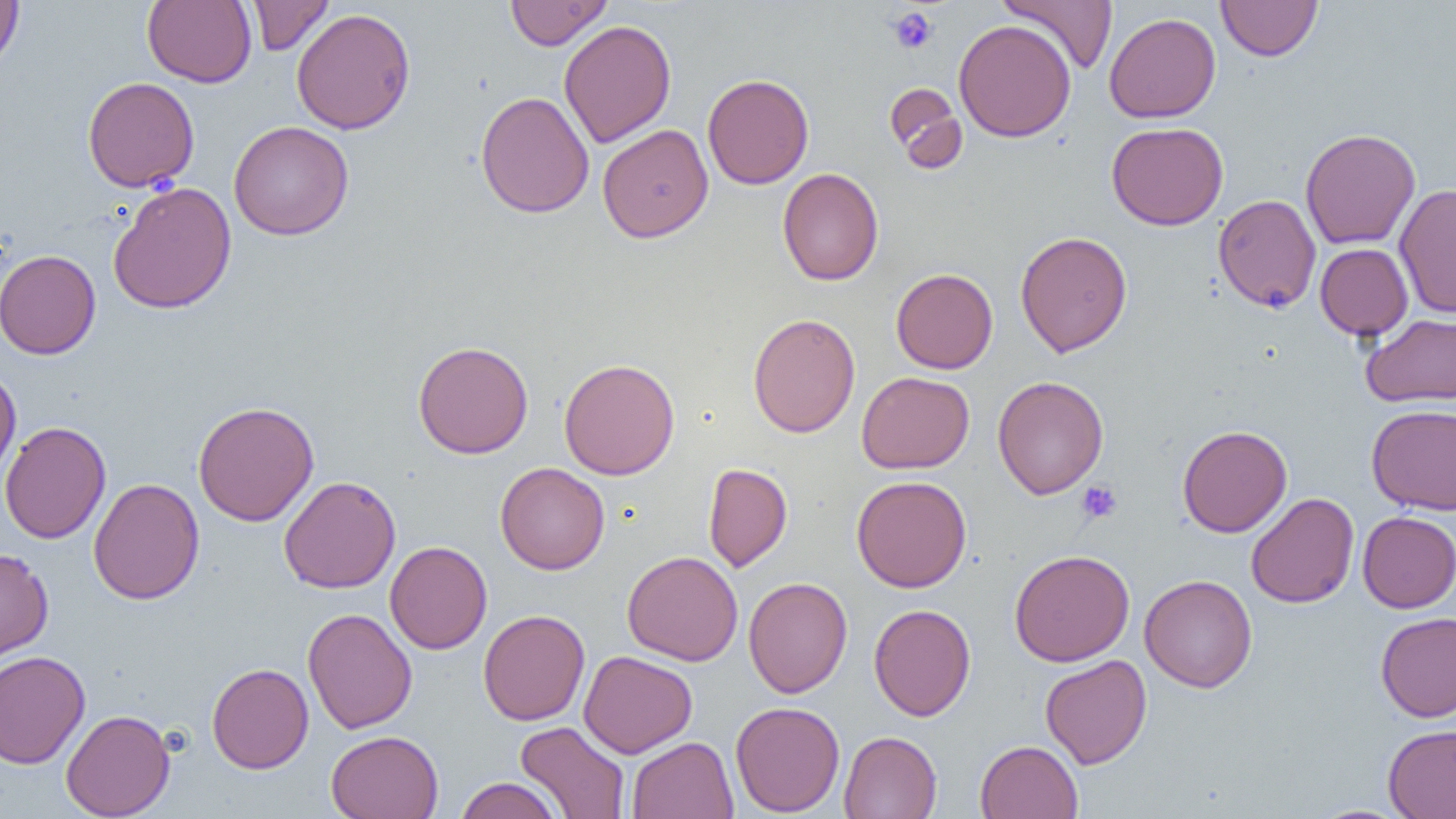

Approximate bounding boxes as [x1, y1, x2, y2] in pixels. Uninfected red blood cell locations: [0, 0, 24, 73], [142, 0, 256, 88], [247, 0, 333, 56], [504, 0, 613, 50], [999, 0, 1118, 74], [1216, 0, 1323, 61], [291, 8, 416, 134], [1104, 12, 1221, 123], [953, 18, 1076, 143], [559, 20, 676, 148], [702, 73, 814, 189], [82, 76, 200, 193], [885, 82, 968, 173], [475, 91, 595, 218], [228, 120, 354, 241], [1106, 122, 1228, 230], [597, 124, 713, 242], [1300, 128, 1421, 250], [777, 168, 884, 286], [108, 181, 236, 314], [1395, 182, 1456, 318], [1213, 193, 1321, 313], [1015, 230, 1132, 357], [1315, 243, 1413, 341], [0, 249, 101, 360], [891, 268, 998, 374], [748, 313, 860, 438], [1361, 313, 1456, 407], [412, 340, 533, 459], [559, 357, 680, 480], [0, 368, 21, 490], [857, 371, 974, 473], [992, 375, 1108, 499], [193, 401, 319, 526], [1366, 404, 1456, 515], [0, 420, 112, 543], [1177, 425, 1292, 537], [495, 462, 609, 574], [703, 462, 793, 572], [851, 475, 972, 593], [278, 476, 401, 593], [88, 478, 204, 604], [1246, 492, 1359, 608], [1357, 511, 1456, 613], [384, 540, 492, 654], [0, 547, 54, 663], [1009, 549, 1134, 666], [622, 550, 743, 666], [1139, 574, 1257, 693], [743, 577, 852, 698], [868, 604, 976, 721], [302, 607, 417, 734], [478, 609, 590, 726], [1375, 611, 1456, 722], [0, 650, 91, 769], [579, 650, 697, 758], [1040, 654, 1152, 769], [207, 662, 313, 773], [730, 701, 844, 817], [61, 709, 175, 818], [514, 721, 630, 818], [1383, 724, 1456, 819], [326, 730, 444, 819], [839, 731, 942, 818], [626, 736, 738, 819], [974, 740, 1083, 818], [454, 777, 563, 819]. Platelet locations: [889, 7, 937, 55], [1077, 481, 1122, 524]. Slide-level diagnosis: no evidence of blood parasites. One field of a larger specimen. Optical microscopy. Image is 1456×819 pixels. Thin blood smear. 1000x magnification.